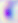
Micrograph. Captured at 400x magnification. Toxoplasma gondii is shown.